Locate every blood parasite and identify its species.
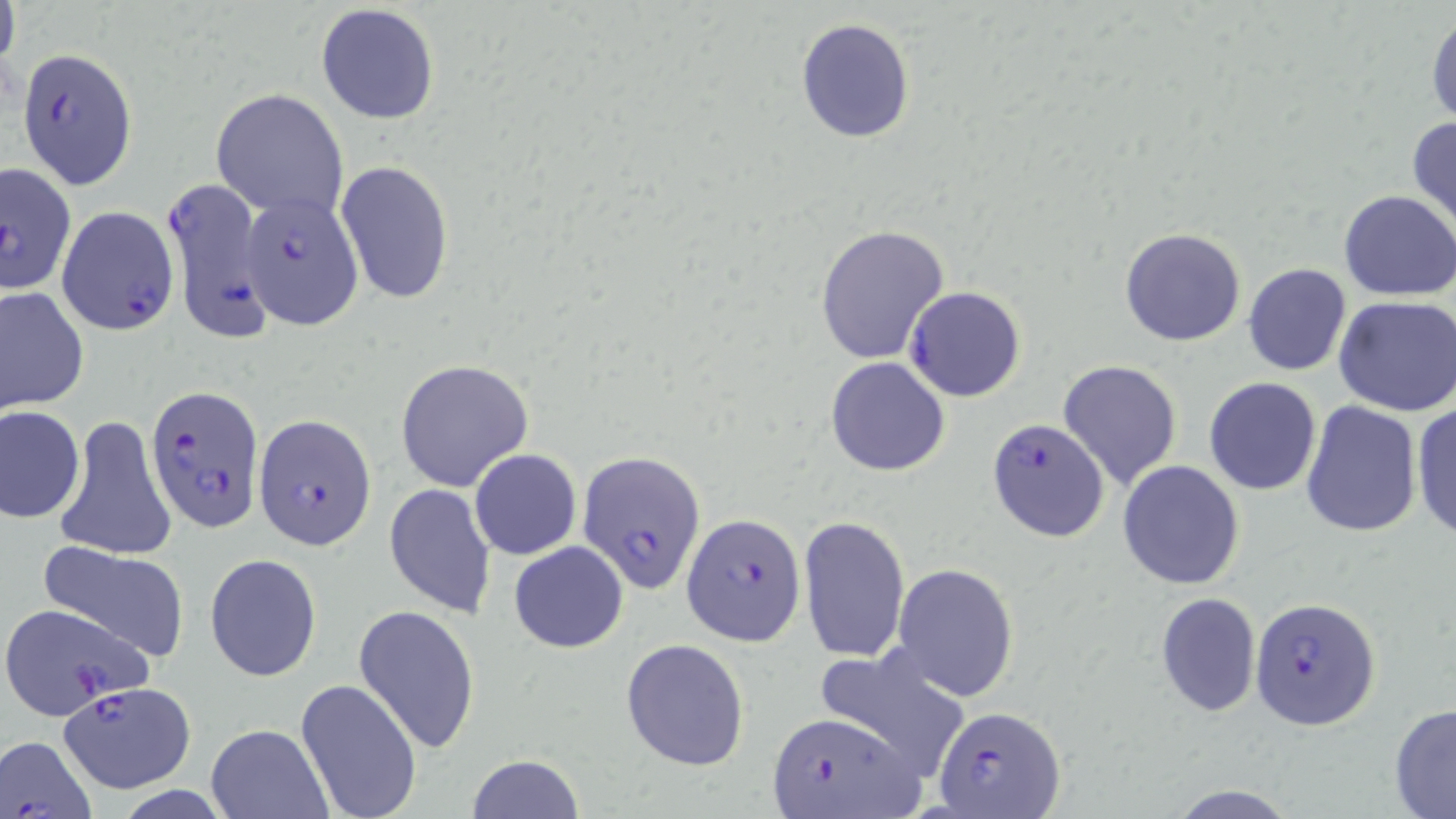
Approximate bounding boxes as named x1/y1/x2/y2 corners in pixels.
Plasmodium falciparum-infected red blood cells (subset): (x1=16, y1=48, x2=137, y2=189), (x1=161, y1=174, x2=272, y2=343), (x1=240, y1=192, x2=363, y2=328), (x1=58, y1=206, x2=178, y2=336), (x1=905, y1=285, x2=1027, y2=402), (x1=146, y1=385, x2=261, y2=533), (x1=255, y1=415, x2=377, y2=550), (x1=985, y1=415, x2=1108, y2=541), (x1=579, y1=450, x2=702, y2=592), (x1=682, y1=512, x2=806, y2=646), (x1=1250, y1=597, x2=1380, y2=730), (x1=1, y1=601, x2=155, y2=719), (x1=59, y1=681, x2=195, y2=792), (x1=935, y1=704, x2=1066, y2=818), (x1=765, y1=709, x2=922, y2=818).
No Plasmodium ovale, Plasmodium malariae, Plasmodium vivax, Babesia divergens, or Trypanosoma brucei observed.

{
  "slide_level_diagnosis": "Plasmodium falciparum",
  "modality": "optical microscopy",
  "preparation": "thin blood smear",
  "uninfected_red_blood_cell_locations_subset": "approximate bounding boxes as named x1/y1/x2/y2 corners in pixels: (x1=0, y1=2, x2=22, y2=86), (x1=315, y1=5, x2=440, y2=125), (x1=1426, y1=14, x2=1456, y2=126), (x1=795, y1=19, x2=915, y2=142), (x1=211, y1=88, x2=350, y2=221), (x1=1407, y1=114, x2=1456, y2=234), (x1=336, y1=160, x2=456, y2=305), (x1=1338, y1=190, x2=1456, y2=301), (x1=815, y1=223, x2=949, y2=364), (x1=1120, y1=227, x2=1247, y2=347), (x1=1242, y1=262, x2=1352, y2=377), (x1=0, y1=286, x2=90, y2=414), (x1=1333, y1=296, x2=1456, y2=417), (x1=826, y1=356, x2=949, y2=475), (x1=393, y1=359, x2=533, y2=491), (x1=1058, y1=359, x2=1182, y2=491), (x1=1203, y1=376, x2=1322, y2=496), (x1=1409, y1=399, x2=1456, y2=541), (x1=1300, y1=401, x2=1422, y2=539), (x1=0, y1=405, x2=86, y2=522), (x1=54, y1=414, x2=176, y2=563), (x1=469, y1=448, x2=582, y2=560), (x1=1117, y1=459, x2=1245, y2=590), (x1=384, y1=483, x2=496, y2=619), (x1=798, y1=515, x2=910, y2=662), (x1=34, y1=539, x2=191, y2=661), (x1=508, y1=541, x2=629, y2=653), (x1=204, y1=553, x2=322, y2=682), (x1=892, y1=562, x2=1019, y2=701), (x1=1156, y1=592, x2=1261, y2=717), (x1=353, y1=604, x2=480, y2=755), (x1=620, y1=638, x2=750, y2=770), (x1=810, y1=644, x2=971, y2=778), (x1=294, y1=677, x2=423, y2=819), (x1=1389, y1=703, x2=1456, y2=817), (x1=206, y1=724, x2=332, y2=818), (x1=465, y1=754, x2=584, y2=819)",
  "image_size": "1456×819 pixels",
  "stain": "May-Grünwald-Giemsa",
  "field_of_view": "single",
  "magnification": "1000x"
}